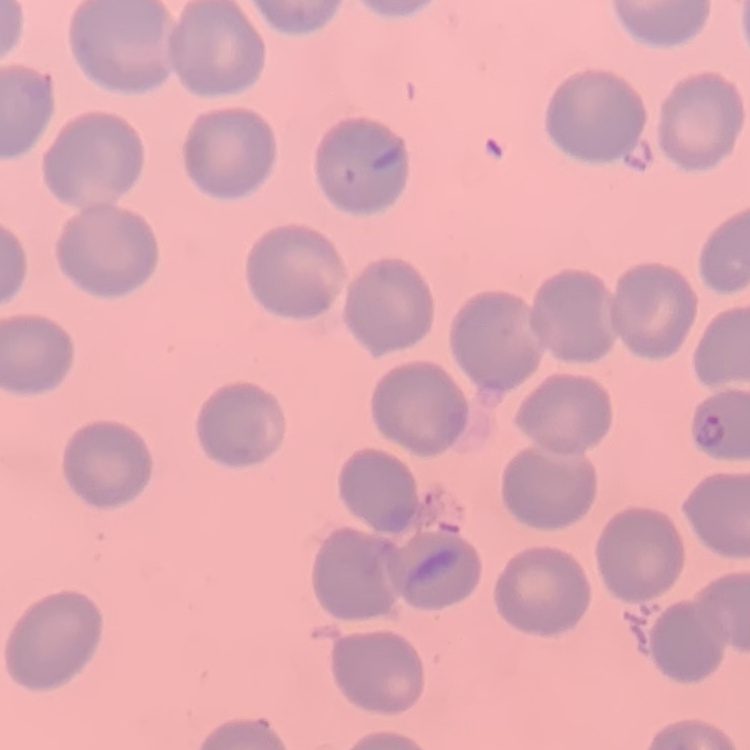
{
  "red_blood_cell_morphology": "no rouleaux formation",
  "preparation": "thin blood film",
  "stain": "Field's or Giemsa",
  "image_type": "one tile cut from a larger photomicrograph"
}